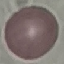

result = no malaria parasites detected
image type = automatically extracted cell patch, resized to 64 × 64 pixels
stain = Giemsa
capture = smartphone through the microscope eyepiece
preparation = thin blood smear